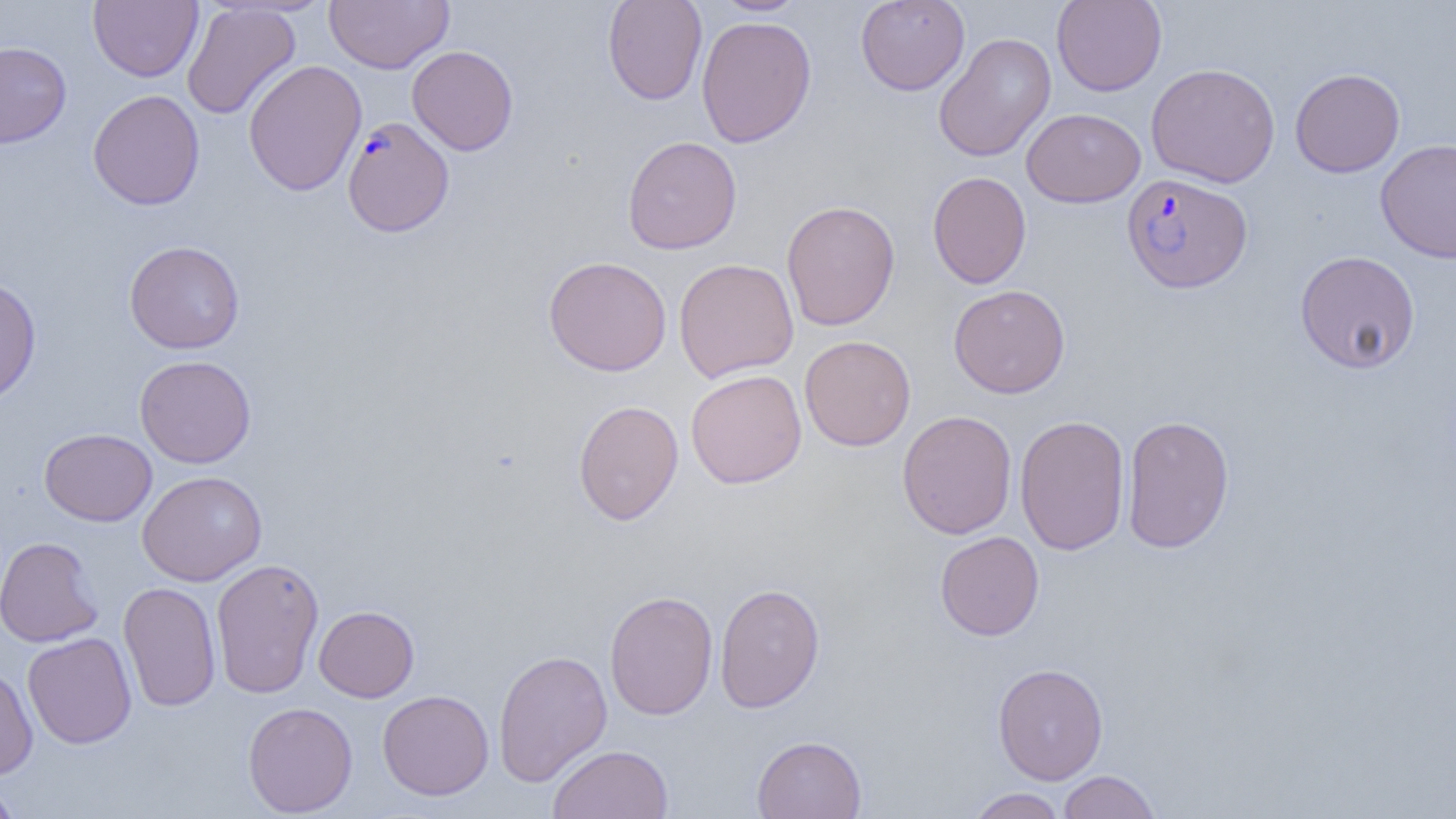

slide-level diagnosis = Plasmodium falciparum
preparation = thin blood film
image size = 1456×819 pixels
magnification = 1000x
Plasmodium falciparum-infected red blood cell locations = approximate bounding boxes as (x1,y1)-(x2,y2) corner pairs in pixels: (342,117)-(454,237), (1122,173)-(1252,293)
uninfected red blood cell locations = approximate bounding boxes as (x1,y1)-(x2,y2) corner pairs in pixels: (88,0)-(202,82), (324,0)-(453,74), (602,0)-(708,106), (855,0)-(970,95), (1051,0)-(1167,96), (711,1)-(811,16), (181,2)-(301,120), (696,15)-(816,147), (934,32)-(1056,162), (0,41)-(71,148), (407,45)-(518,155), (243,59)-(367,196), (1145,62)-(1280,188), (1290,68)-(1405,177), (88,89)-(204,210), (1021,108)-(1146,207), (622,135)-(742,254), (1375,139)-(1456,263), (928,171)-(1031,289), (781,200)-(900,331), (124,240)-(245,354), (1294,250)-(1421,374), (543,256)-(673,377), (673,258)-(799,382), (0,276)-(41,407), (948,284)-(1071,398), (799,335)-(916,451), (134,355)-(257,468), (686,369)-(807,489), (573,399)-(684,526), (897,409)-(1017,539), (1121,414)-(1235,554), (1014,415)-(1130,556), (39,428)-(157,526), (137,470)-(267,586), (935,531)-(1044,641), (0,536)-(104,647), (210,557)-(324,698), (118,581)-(221,711), (714,583)-(825,713), (604,590)-(718,721), (313,605)-(419,702), (22,632)-(137,749), (493,648)-(613,786), (992,663)-(1108,785), (0,665)-(38,780), (377,689)-(494,800), (242,702)-(358,816), (751,735)-(867,819), (547,743)-(673,819), (1057,770)-(1161,819), (0,781)-(22,819), (966,787)-(1068,818)
field of view = single
modality = light microscopy